Assess the morphology of the erythrocytes.
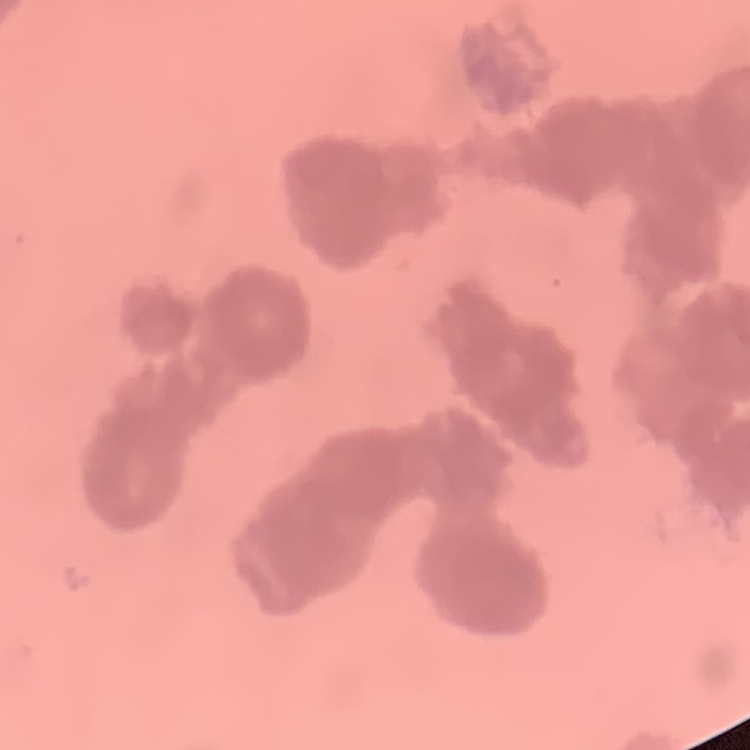

They show rouleaux formation.

Summary:
  - Image type: square crop of a larger photomicrograph
  - Preparation: thin blood film
  - Stain: Field's or Giemsa